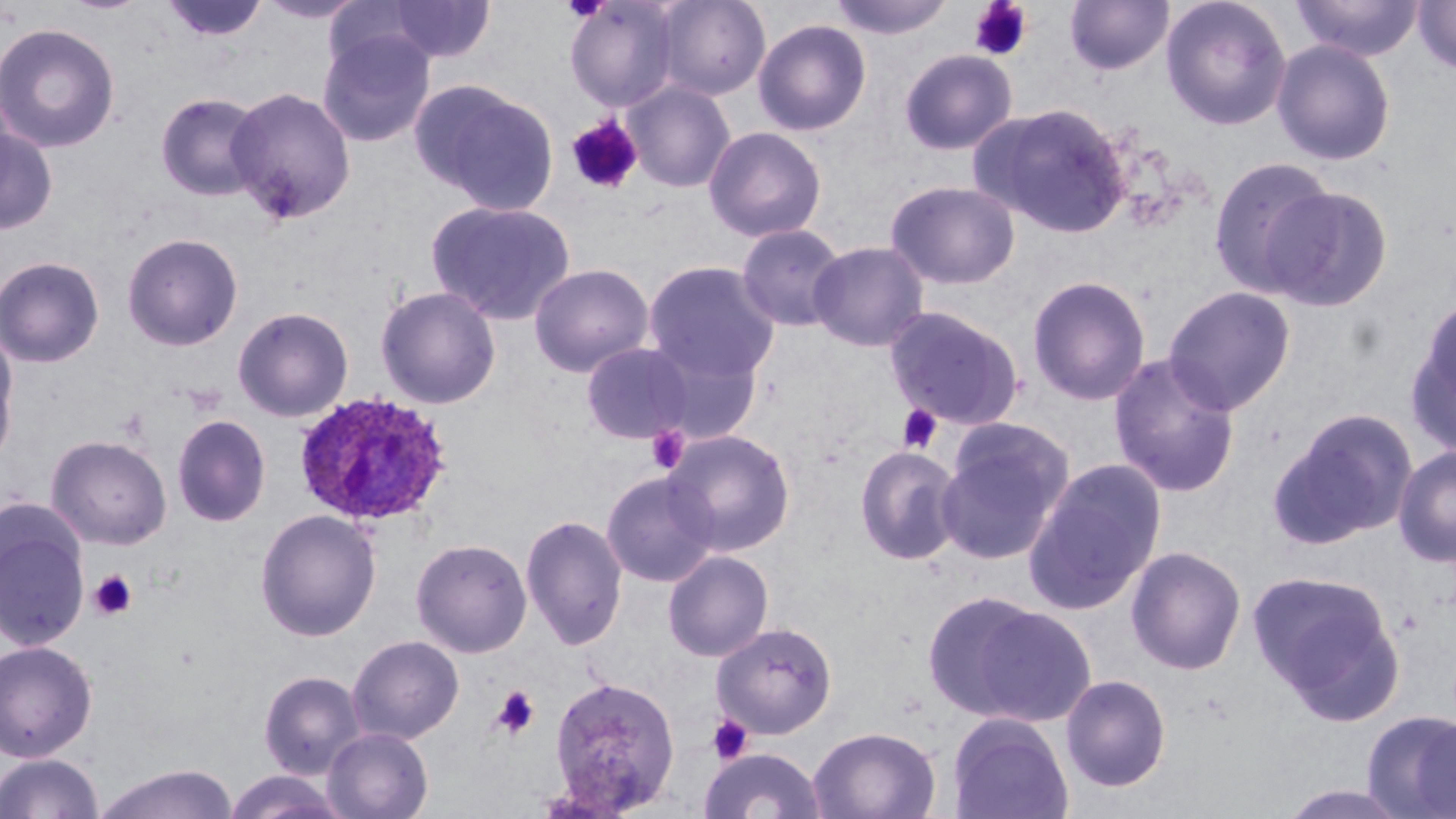
slide-level diagnosis = Plasmodium ovale
platelet locations = approximate bounding boxes as named x1/y1/x2/y2 corners in pixels: (x1=562, y1=0, x2=610, y2=23), (x1=969, y1=0, x2=1034, y2=61), (x1=565, y1=114, x2=644, y2=195), (x1=897, y1=404, x2=943, y2=454), (x1=646, y1=425, x2=690, y2=474), (x1=89, y1=569, x2=138, y2=621), (x1=490, y1=686, x2=540, y2=739), (x1=707, y1=714, x2=753, y2=764)
uninfected red blood cell locations = approximate bounding boxes as named x1/y1/x2/y2 corners in pixels: (x1=160, y1=0, x2=269, y2=43), (x1=256, y1=0, x2=367, y2=25), (x1=655, y1=0, x2=771, y2=101), (x1=827, y1=0, x2=956, y2=40), (x1=1064, y1=0, x2=1174, y2=76), (x1=1160, y1=0, x2=1293, y2=131), (x1=1291, y1=0, x2=1425, y2=61), (x1=377, y1=1, x2=496, y2=64), (x1=564, y1=1, x2=681, y2=113), (x1=1412, y1=1, x2=1456, y2=75), (x1=753, y1=19, x2=872, y2=136), (x1=0, y1=22, x2=121, y2=153), (x1=317, y1=29, x2=436, y2=147), (x1=1271, y1=39, x2=1397, y2=166), (x1=898, y1=49, x2=1018, y2=155), (x1=622, y1=81, x2=735, y2=193), (x1=412, y1=82, x2=558, y2=214), (x1=224, y1=86, x2=357, y2=225), (x1=155, y1=92, x2=266, y2=202), (x1=977, y1=103, x2=1132, y2=237), (x1=0, y1=118, x2=58, y2=235), (x1=703, y1=126, x2=827, y2=243), (x1=1207, y1=155, x2=1337, y2=298), (x1=886, y1=180, x2=1021, y2=290), (x1=1264, y1=185, x2=1393, y2=312), (x1=426, y1=200, x2=577, y2=325), (x1=736, y1=223, x2=848, y2=333), (x1=122, y1=232, x2=243, y2=351), (x1=808, y1=241, x2=929, y2=352), (x1=0, y1=255, x2=105, y2=368), (x1=643, y1=260, x2=780, y2=384), (x1=528, y1=263, x2=654, y2=377), (x1=1027, y1=275, x2=1151, y2=406), (x1=375, y1=285, x2=501, y2=409), (x1=1162, y1=285, x2=1297, y2=416), (x1=1407, y1=299, x2=1456, y2=454), (x1=884, y1=305, x2=1026, y2=431), (x1=232, y1=306, x2=354, y2=422), (x1=0, y1=332, x2=19, y2=466), (x1=641, y1=339, x2=765, y2=446), (x1=581, y1=342, x2=693, y2=444), (x1=1108, y1=352, x2=1241, y2=499), (x1=1275, y1=407, x2=1418, y2=546), (x1=172, y1=415, x2=271, y2=527), (x1=938, y1=418, x2=1074, y2=563), (x1=663, y1=429, x2=796, y2=557), (x1=46, y1=435, x2=172, y2=549), (x1=854, y1=444, x2=964, y2=566), (x1=1393, y1=445, x2=1456, y2=566), (x1=1024, y1=459, x2=1166, y2=613), (x1=601, y1=471, x2=720, y2=587), (x1=0, y1=507, x2=91, y2=653), (x1=255, y1=508, x2=382, y2=642), (x1=521, y1=513, x2=627, y2=650), (x1=410, y1=538, x2=532, y2=658), (x1=1126, y1=545, x2=1247, y2=675), (x1=662, y1=550, x2=774, y2=662), (x1=1248, y1=569, x2=1404, y2=721), (x1=921, y1=591, x2=1052, y2=721), (x1=968, y1=604, x2=1097, y2=727), (x1=712, y1=621, x2=838, y2=739), (x1=347, y1=635, x2=465, y2=744), (x1=0, y1=640, x2=98, y2=761), (x1=259, y1=670, x2=366, y2=779), (x1=1060, y1=673, x2=1172, y2=793), (x1=548, y1=674, x2=681, y2=813), (x1=1362, y1=709, x2=1456, y2=818), (x1=947, y1=713, x2=1074, y2=819), (x1=808, y1=725, x2=941, y2=819), (x1=322, y1=726, x2=434, y2=819), (x1=699, y1=747, x2=827, y2=819), (x1=0, y1=752, x2=103, y2=818), (x1=93, y1=763, x2=239, y2=819), (x1=221, y1=770, x2=352, y2=819)
Plasmodium ovale-infected red blood cell locations = approximate bounding boxes as named x1/y1/x2/y2 corners in pixels: (x1=293, y1=390, x2=454, y2=528)
stain = May-Grünwald-Giemsa
field of view = one of a larger specimen
preparation = thin blood smear
image size = 1456×819 pixels
modality = optical microscopy
magnification = 1000x